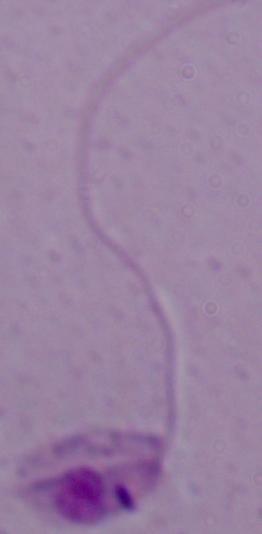
1000x magnification. A Leishmania parasite is shown. Micrograph.